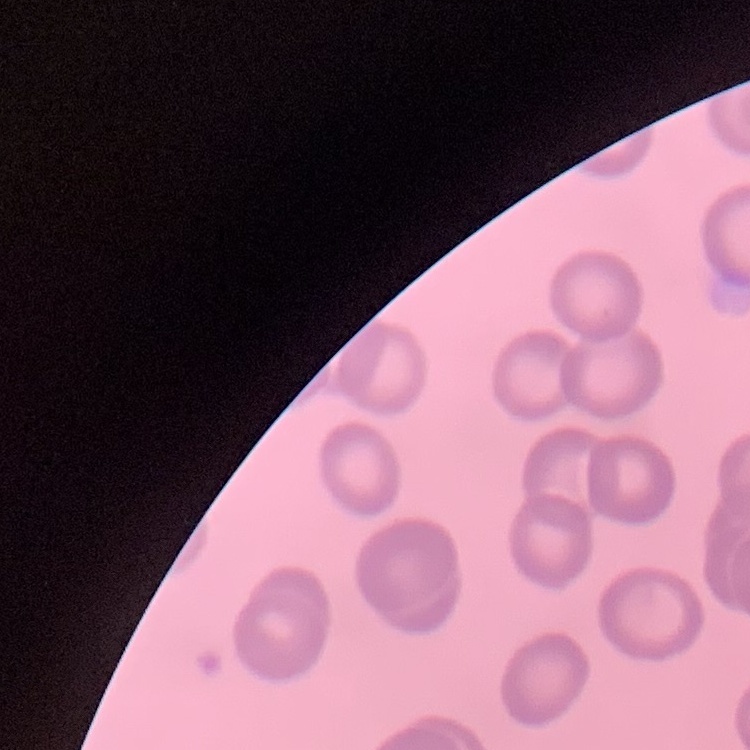
Summary:
  - Red blood cell morphology: no rouleaux formation
  - Preparation: thin blood smear
  - Image type: square crop of a larger photomicrograph
  - Stain: Field's or Giemsa